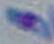

identification = Toxoplasma gondii
modality = photomicrograph
magnification = 1000x